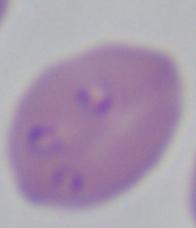
Summary:
  - Modality: micrograph
  - Identification: Babesia
  - Magnification: 1000x